Describe the morphology of the erythrocytes.
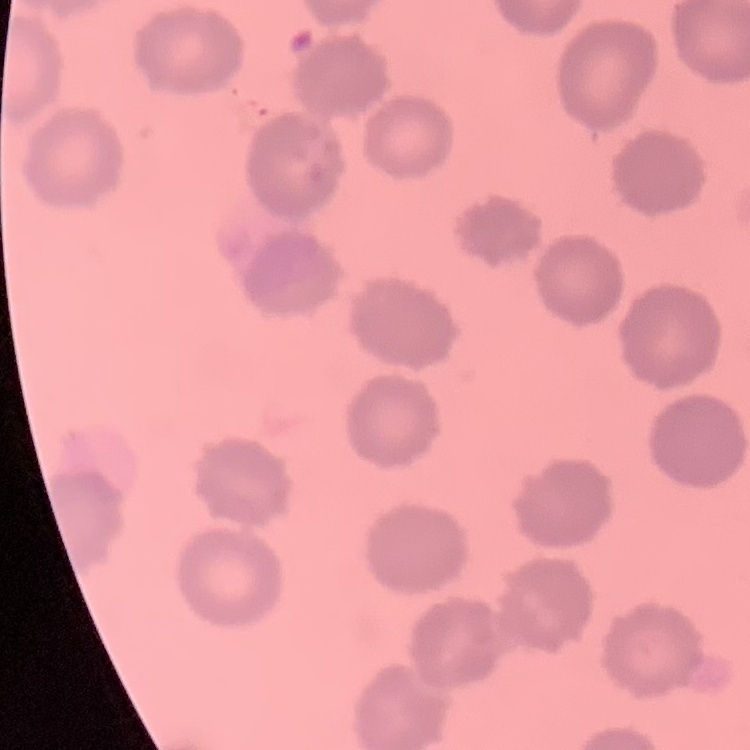
No rouleaux formation.

Summary:
  - Stain: Field's or Giemsa
  - Preparation: thin blood smear
  - Image type: square crop of a larger photomicrograph